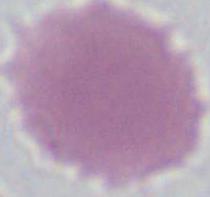

A red blood cell is shown. Photomicrograph. 1000x magnification.